Classify this cell by malaria status.
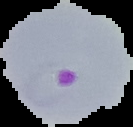
Parasitized.

image size = 133×127 pixels
image type = cell region segmented out of the field of view; surrounding area masked to black
preparation = thin blood film